Mark where platelets are.
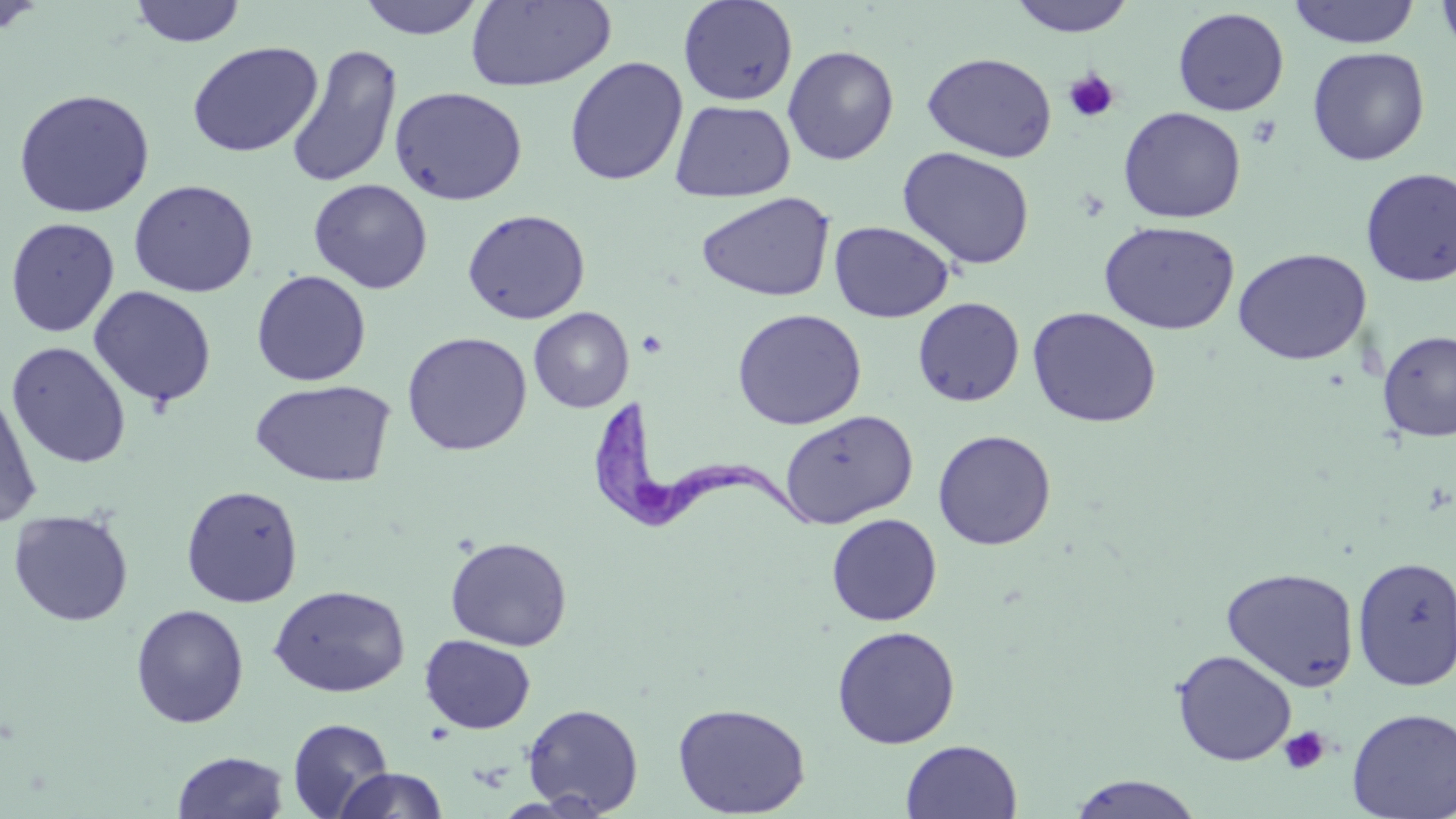

Approximate bounding boxes as [x1, y1, x2, y2] in pixels.
Platelets: [1063, 68, 1120, 123], [637, 329, 669, 359], [1278, 726, 1330, 775].

{
  "slide_level_diagnosis": "Trypanosoma brucei",
  "field_of_view": "single",
  "stain": "May-Grünwald-Giemsa",
  "uninfected_red_blood_cell_locations": "approximate bounding boxes as [x1, y1, x2, y2] in pixels: [129, 0, 246, 47], [357, 0, 487, 39], [466, 0, 617, 92], [678, 0, 798, 105], [1007, 0, 1137, 37], [1288, 0, 1420, 48], [1436, 0, 1456, 56], [0, 2, 49, 37], [1172, 7, 1290, 116], [187, 41, 323, 157], [285, 44, 403, 189], [782, 45, 900, 166], [1307, 46, 1430, 166], [922, 52, 1058, 162], [564, 56, 688, 186], [389, 86, 528, 206], [14, 88, 155, 218], [670, 100, 796, 202], [1118, 106, 1246, 224], [897, 146, 1036, 270], [1359, 167, 1456, 287], [128, 179, 258, 298], [308, 179, 433, 294], [696, 191, 835, 302], [462, 208, 591, 324], [4, 217, 120, 338], [828, 220, 954, 323], [1099, 220, 1240, 335], [1233, 247, 1371, 364], [251, 270, 372, 386], [88, 286, 217, 408], [913, 297, 1025, 407], [1027, 306, 1162, 428], [529, 307, 634, 412], [731, 308, 867, 430], [1377, 330, 1456, 442], [401, 331, 533, 456], [6, 341, 131, 468], [249, 379, 396, 487], [0, 385, 43, 527], [779, 409, 918, 529], [932, 429, 1056, 550], [181, 484, 304, 608], [7, 509, 134, 627], [826, 513, 942, 626], [445, 536, 572, 651], [1352, 555, 1456, 691], [1221, 567, 1360, 691], [268, 585, 410, 698], [130, 604, 249, 728], [831, 625, 960, 748], [419, 634, 536, 734], [1171, 649, 1297, 766], [672, 702, 811, 817], [522, 703, 644, 816], [1345, 707, 1456, 818], [287, 717, 394, 818], [901, 739, 1023, 819], [173, 750, 289, 818], [332, 767, 449, 818], [1064, 774, 1206, 818]",
  "image_size": "1456×819 pixels",
  "modality": "optical microscopy",
  "trypanosoma_brucei_locations": "approximate bounding boxes as [x1, y1, x2, y2] in pixels: [598, 406, 820, 533]",
  "magnification": "1000x",
  "preparation": "thin blood film"
}